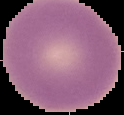
Image is 124×115 pixels. From a thin blood smear. Malaria status: uninfected. Segmented cell region on a black background.